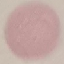
Summary:
  - Malaria status: uninfected
  - Image type: cell patch, automatically extracted from a larger field of view and resized to 64 × 64 pixels
  - Preparation: thin blood film
  - Capture: smartphone camera at the microscope eyepiece
  - Stain: Giemsa